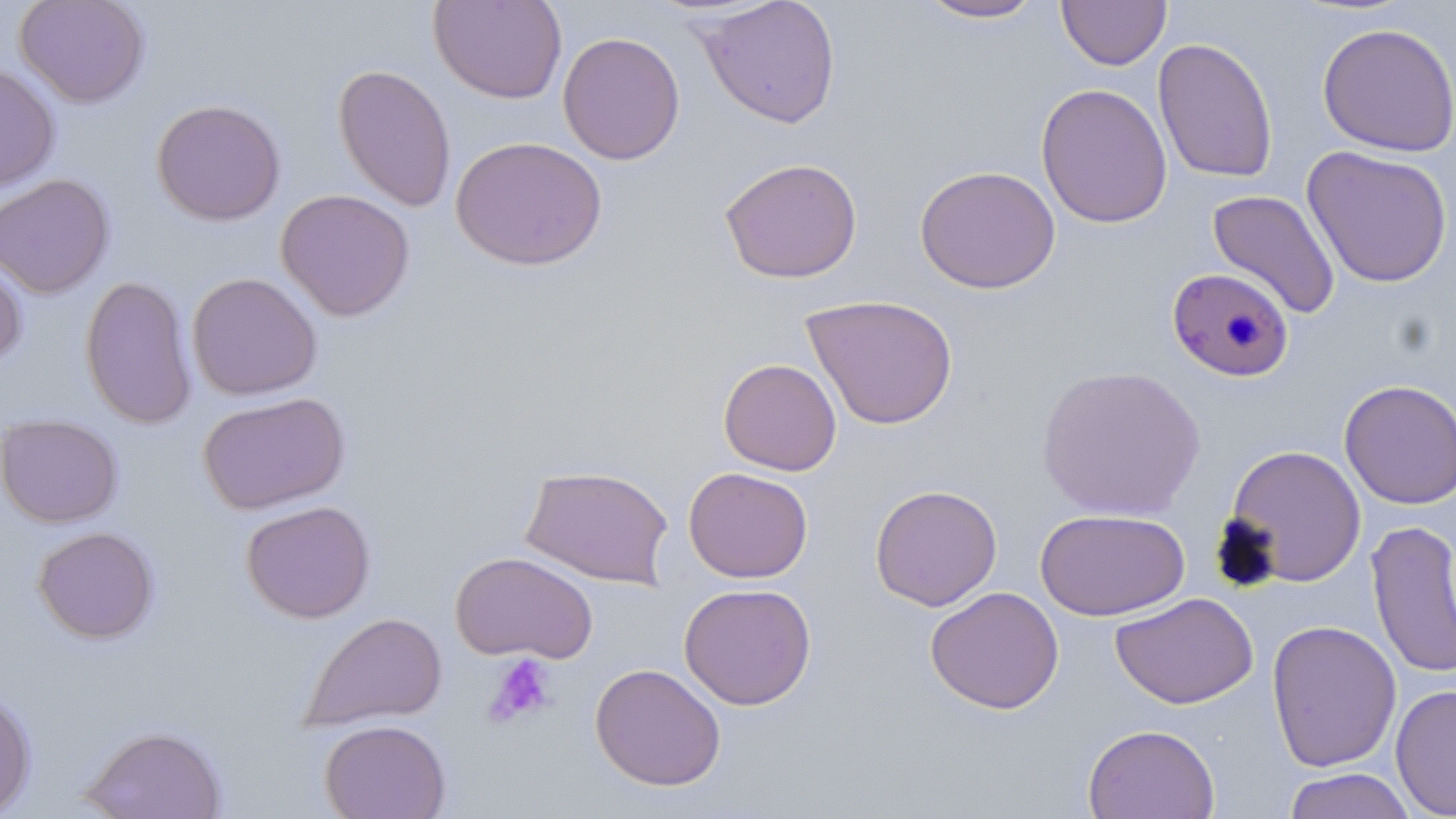 Approximate bounding boxes as named x1/y1/x2/y2 corners in pixels. Platelet locations: (x1=484, y1=654, x2=557, y2=727). Uninfected red blood cell locations: (x1=13, y1=0, x2=150, y2=108), (x1=428, y1=0, x2=567, y2=104), (x1=695, y1=0, x2=841, y2=129), (x1=1057, y1=0, x2=1171, y2=70), (x1=914, y1=1, x2=1048, y2=23), (x1=1317, y1=22, x2=1456, y2=157), (x1=557, y1=32, x2=686, y2=165), (x1=1152, y1=37, x2=1279, y2=184), (x1=0, y1=62, x2=60, y2=193), (x1=332, y1=63, x2=457, y2=213), (x1=1035, y1=82, x2=1173, y2=229), (x1=151, y1=99, x2=286, y2=226), (x1=450, y1=136, x2=608, y2=271), (x1=1302, y1=146, x2=1453, y2=288), (x1=720, y1=157, x2=863, y2=283), (x1=915, y1=165, x2=1061, y2=294), (x1=0, y1=173, x2=115, y2=299), (x1=276, y1=189, x2=415, y2=321), (x1=1206, y1=189, x2=1341, y2=320), (x1=0, y1=251, x2=28, y2=369), (x1=187, y1=272, x2=323, y2=401), (x1=79, y1=274, x2=198, y2=430), (x1=801, y1=294, x2=959, y2=430), (x1=718, y1=357, x2=842, y2=476), (x1=1036, y1=364, x2=1206, y2=521), (x1=1339, y1=379, x2=1456, y2=510), (x1=198, y1=392, x2=350, y2=515), (x1=0, y1=414, x2=123, y2=527), (x1=1224, y1=444, x2=1367, y2=587), (x1=519, y1=464, x2=675, y2=588), (x1=683, y1=466, x2=813, y2=583), (x1=869, y1=483, x2=1002, y2=611), (x1=241, y1=500, x2=376, y2=623), (x1=1034, y1=508, x2=1190, y2=621), (x1=1365, y1=519, x2=1456, y2=680), (x1=32, y1=526, x2=159, y2=643), (x1=450, y1=550, x2=598, y2=664), (x1=678, y1=582, x2=817, y2=710), (x1=925, y1=586, x2=1065, y2=714), (x1=1110, y1=592, x2=1258, y2=709), (x1=299, y1=611, x2=448, y2=731), (x1=1265, y1=619, x2=1402, y2=772), (x1=589, y1=662, x2=726, y2=791), (x1=1390, y1=684, x2=1456, y2=817), (x1=0, y1=688, x2=36, y2=818), (x1=319, y1=718, x2=451, y2=819), (x1=1082, y1=723, x2=1220, y2=819), (x1=80, y1=724, x2=228, y2=819), (x1=1281, y1=768, x2=1417, y2=819). Plasmodium falciparum-infected red blood cell locations: (x1=1166, y1=267, x2=1295, y2=382). Slide-level diagnosis: Plasmodium falciparum. Image is 1456×819 pixels. One field of a larger specimen. May-Grünwald-Giemsa-stained preparation. Captured at 1000x magnification. Optical microscopy. Thin blood film.